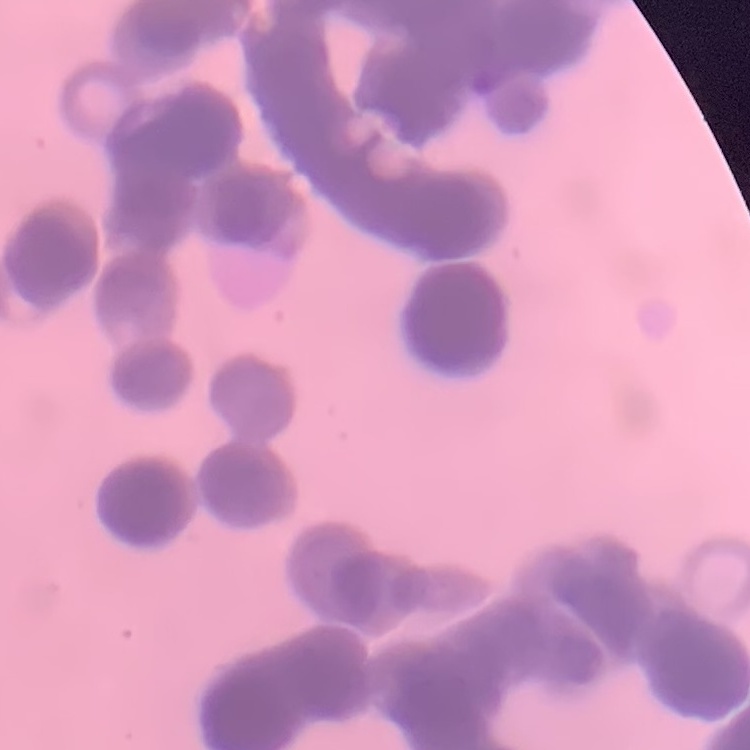
Summary:
  - Red blood cell morphology: rouleaux formation
  - Preparation: thin blood smear
  - Stain: Field's or Giemsa
  - Image type: square crop of a larger photomicrograph